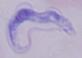
Summary:
  - Modality: photomicrograph
  - Magnification: 1000x
  - Identification: trypanosome